Locate every Plasmodium parasite.
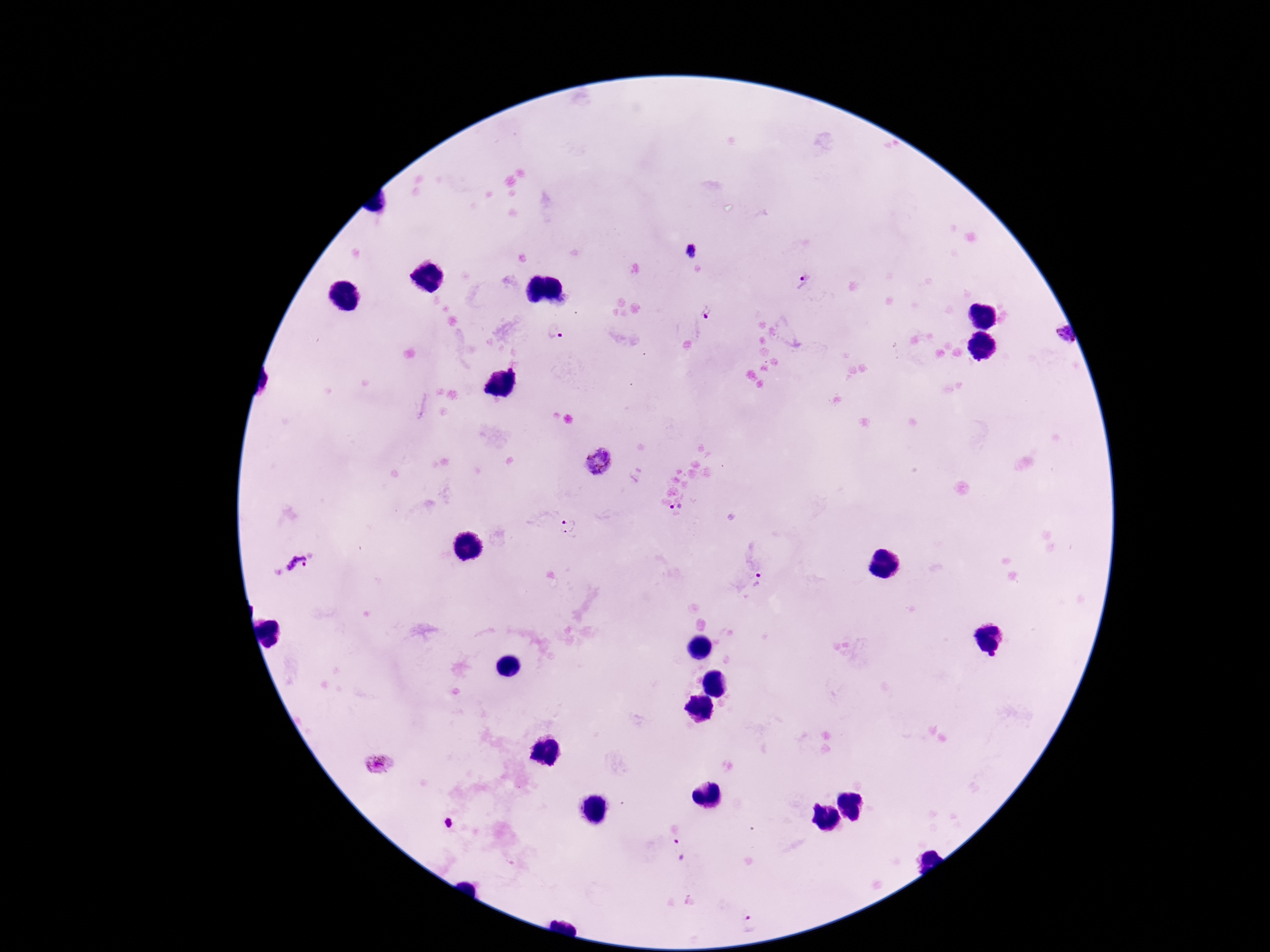

Approximate centers as {x, y} in pixels.
Plasmodium parasites: {692, 251}, {802, 281}, {707, 310}, {554, 332}, {1057, 336}, {597, 460}, {676, 507}, {568, 526}, {298, 566}, {759, 581}, {378, 764}, {448, 824}, {678, 848}, {749, 926}.

Summary:
  - Preparation: thick blood smear
  - Image size: 1270×952 pixels
  - Capture: smartphone camera through the microscope eyepiece
  - Stain: Giemsa
  - Field of view: single
  - Patient malaria status: positive
  - Magnification: 100x